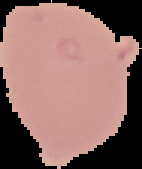
Image is 142×169 pixels. Result: negative for Plasmodium parasites. Segmented cell region on a black background. From a thin blood film.